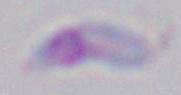

Summary:
  - Identification: Toxoplasma gondii
  - Modality: photomicrograph
  - Magnification: 1000x